Locate and identify every blood parasite.
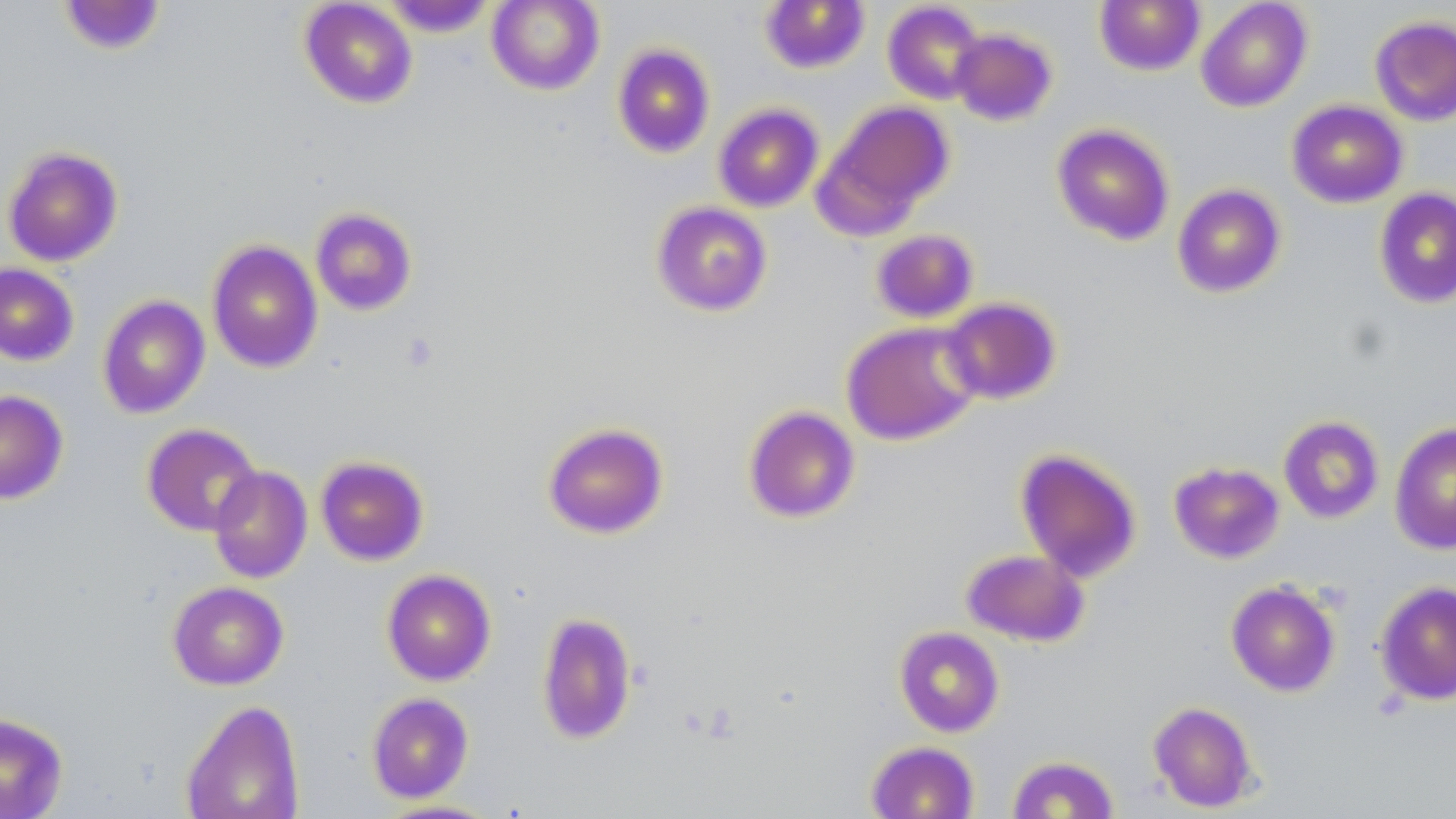
No blood parasites observed.

{
  "slide_level_diagnosis": "no evidence of blood parasites",
  "field_of_view": "one of a larger specimen",
  "modality": "optical microscopy",
  "image_size": "1456×819 pixels",
  "preparation": "thin blood smear",
  "magnification": "1000x",
  "stain": "May-Grünwald-Giemsa",
  "uninfected_red_blood_cell_locations": "approximate bounding boxes as (x1,y1)-(x2,y2) corner pairs in pixels: (486,0)-(605,95), (760,0)-(870,74), (1196,0)-(1312,112), (58,1)-(168,56), (299,1)-(418,109), (379,1)-(498,37), (882,1)-(987,105), (1094,1)-(1205,75), (1369,15)-(1456,126), (949,27)-(1058,126), (612,43)-(715,158), (823,100)-(954,224), (1286,100)-(1408,208), (713,103)-(824,212), (1051,123)-(1175,246), (2,145)-(123,267), (1172,183)-(1286,298), (1373,187)-(1456,310), (651,201)-(772,316), (309,206)-(418,316), (871,228)-(979,323), (206,239)-(323,374), (0,263)-(79,366), (97,294)-(210,419), (941,297)-(1061,404), (841,320)-(982,446), (0,389)-(69,504), (743,406)-(861,524), (1278,415)-(1384,523), (542,421)-(669,539), (1389,422)-(1456,555), (142,423)-(262,536), (1015,448)-(1142,582), (315,455)-(430,566), (1168,461)-(1285,564), (208,466)-(313,583), (961,548)-(1089,647), (381,568)-(496,686), (1226,580)-(1341,697), (1374,580)-(1456,706), (167,581)-(289,690), (536,612)-(637,745), (894,626)-(1004,737), (366,692)-(474,803), (180,699)-(305,819), (1148,701)-(1258,812), (0,712)-(68,818), (865,740)-(980,819), (1007,754)-(1119,818), (373,798)-(506,818)"
}